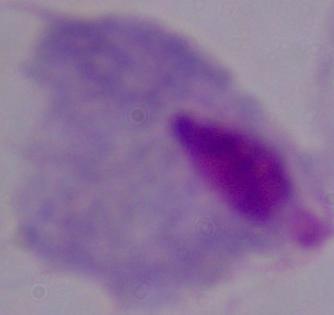
modality: micrograph
magnification: 1000x
identification: trichomonad